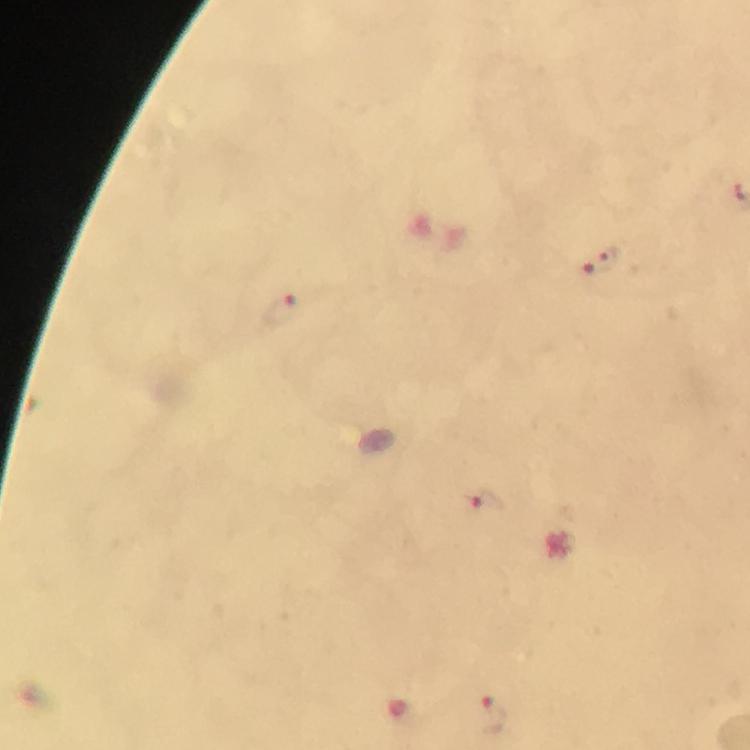

Approximate centers as {x, y} in pixels.
Summary:
  - Plasmodium parasite locations: {610, 256}, {586, 272}, {282, 310}, {486, 503}, {492, 717}
  - Magnification: 100x
  - Cropped from: a single field of view
  - Immersion oil: applied
  - Image size: 750×750 pixels
  - Preparation: thick smear
  - Stain: Giemsa
  - Capture: smartphone mounted on the microscope
  - Context: from a malaria diagnostic workup